Outline each Plasmodium falciparum-infected red blood cell.
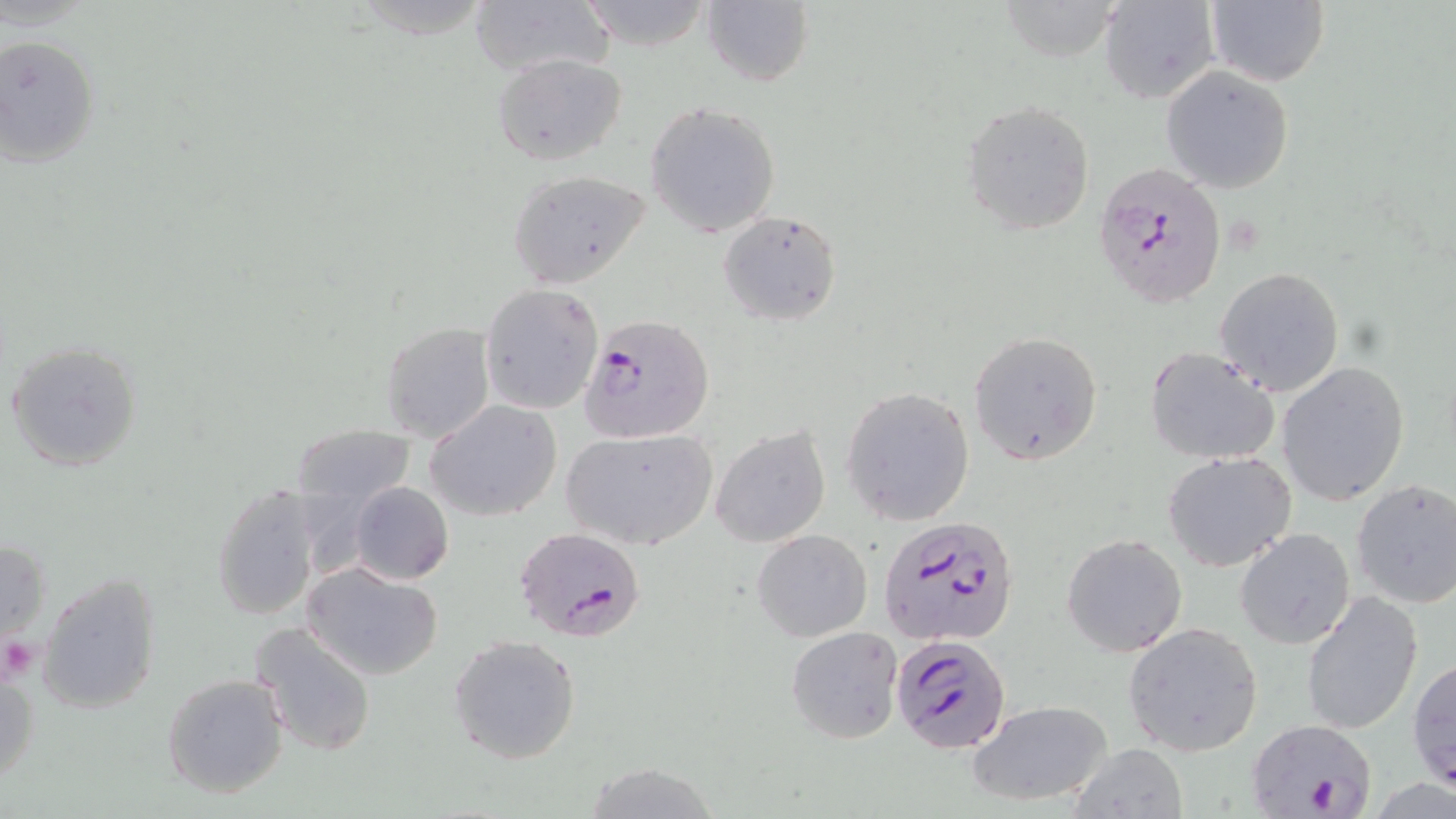

Approximate bounding boxes as (x1,y1)-(x2,y2) corner pairs in pixels.
Plasmodium falciparum-infected red blood cells: (1093,163)-(1227,310), (580,315)-(715,442), (880,514)-(1020,648), (514,524)-(648,644), (891,634)-(1012,753), (1247,718)-(1378,819).

Summary:
  - Uninfected red blood cell locations: (466,0)-(615,81), (575,0)-(716,51), (701,0)-(814,88), (994,0)-(1123,63), (1098,0)-(1220,105), (1205,0)-(1329,87), (0,34)-(102,168), (494,55)-(627,166), (1161,67)-(1294,192), (961,100)-(1096,235), (645,101)-(783,238), (506,168)-(651,289), (718,209)-(843,325), (1214,266)-(1345,396), (480,283)-(603,414), (379,322)-(495,444), (968,331)-(1104,468), (4,340)-(142,472), (1143,346)-(1280,465), (1275,360)-(1411,506), (841,386)-(976,526), (428,400)-(562,522), (291,423)-(415,510), (710,424)-(832,548), (564,427)-(716,552), (1162,450)-(1298,571), (1350,478)-(1456,609), (348,482)-(453,585), (212,483)-(322,620), (752,529)-(871,642), (1235,529)-(1356,649), (1061,533)-(1188,658), (2,535)-(48,648), (302,562)-(446,680), (35,570)-(162,716), (1300,591)-(1424,735), (250,621)-(378,758), (1122,621)-(1264,756), (785,626)-(902,744), (448,633)-(581,765), (1408,657)-(1455,792), (0,669)-(40,785), (160,672)-(291,797), (967,699)-(1113,807), (1066,741)-(1191,819), (581,764)-(719,818)
  - Platelet locations: (1,634)-(41,683)
  - Slide-level diagnosis: Plasmodium falciparum
  - Preparation: thin blood smear
  - Magnification: 1000x
  - Field of view: one of a larger specimen
  - Modality: optical microscopy
  - Stain: May-Grünwald-Giemsa
  - Image size: 1456×819 pixels